Locate every malaria parasite and every leukocyte.
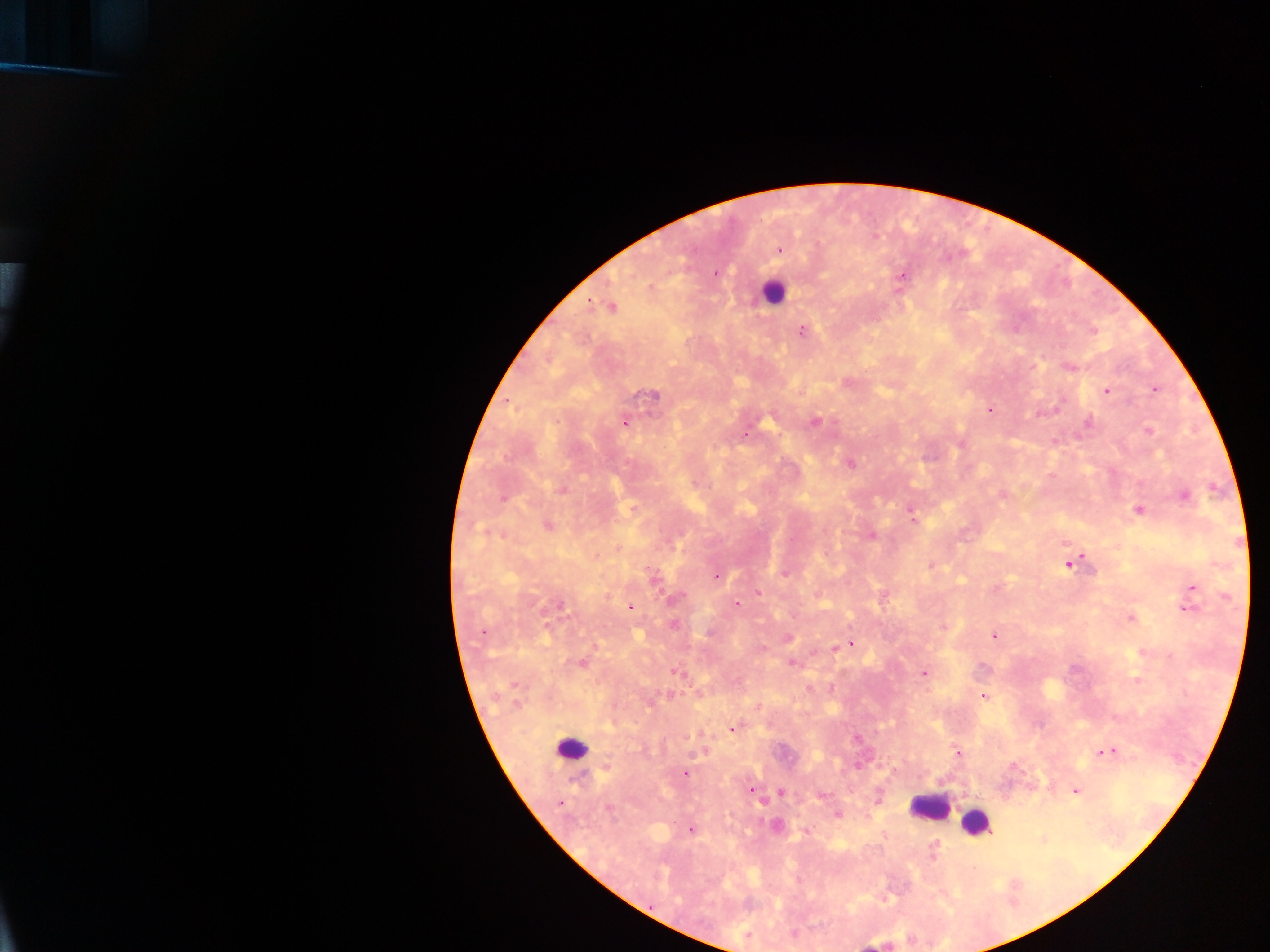

Approximate centers as {x, y} in pixels.
Malaria parasites: {780, 250}, {715, 274}, {903, 275}, {611, 308}, {802, 330}, {1069, 367}, {1154, 389}, {1106, 390}, {653, 397}, {990, 410}, {815, 421}, {625, 423}, {1088, 423}, {1148, 430}, {746, 434}, {961, 444}, {851, 463}, {560, 490}, {1184, 496}, {502, 499}, {1139, 510}, {914, 521}, {547, 526}, {872, 536}, {931, 564}, {1068, 564}, {784, 574}, {716, 577}, {654, 578}, {1193, 587}, {758, 594}, {1227, 596}, {676, 599}, {736, 604}, {559, 606}, {630, 608}, {1187, 609}, {1131, 618}, {673, 625}, {943, 627}, {482, 632}, {994, 636}, {850, 643}, {835, 647}, {792, 663}, {582, 664}, {677, 673}, {923, 674}, {514, 685}, {984, 697}, {649, 701}, {517, 704}, {758, 706}, {733, 729}, {958, 752}, {1109, 752}, {684, 773}, {751, 790}, {782, 792}, {1075, 792}, {823, 795}, {561, 802}, {608, 809}, {838, 815}, {775, 826}, {691, 831}, {807, 832}, {933, 854}.
Leukocytes: {773, 291}, {572, 748}, {928, 807}, {975, 823}, {873, 944}.

Collected in Ghana. Thick blood smear. One field of view. Image is 1270×952 pixels. Mobile-phone photograph taken through the microscope.